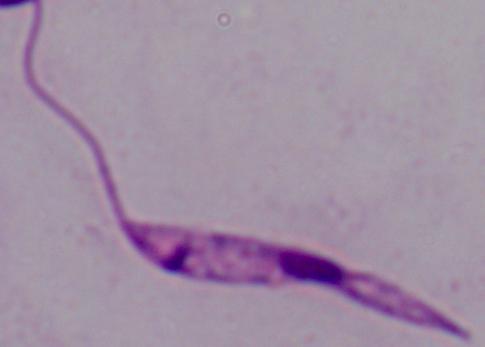
Photomicrograph. Captured at 1000x magnification. A Leishmania parasite is shown.